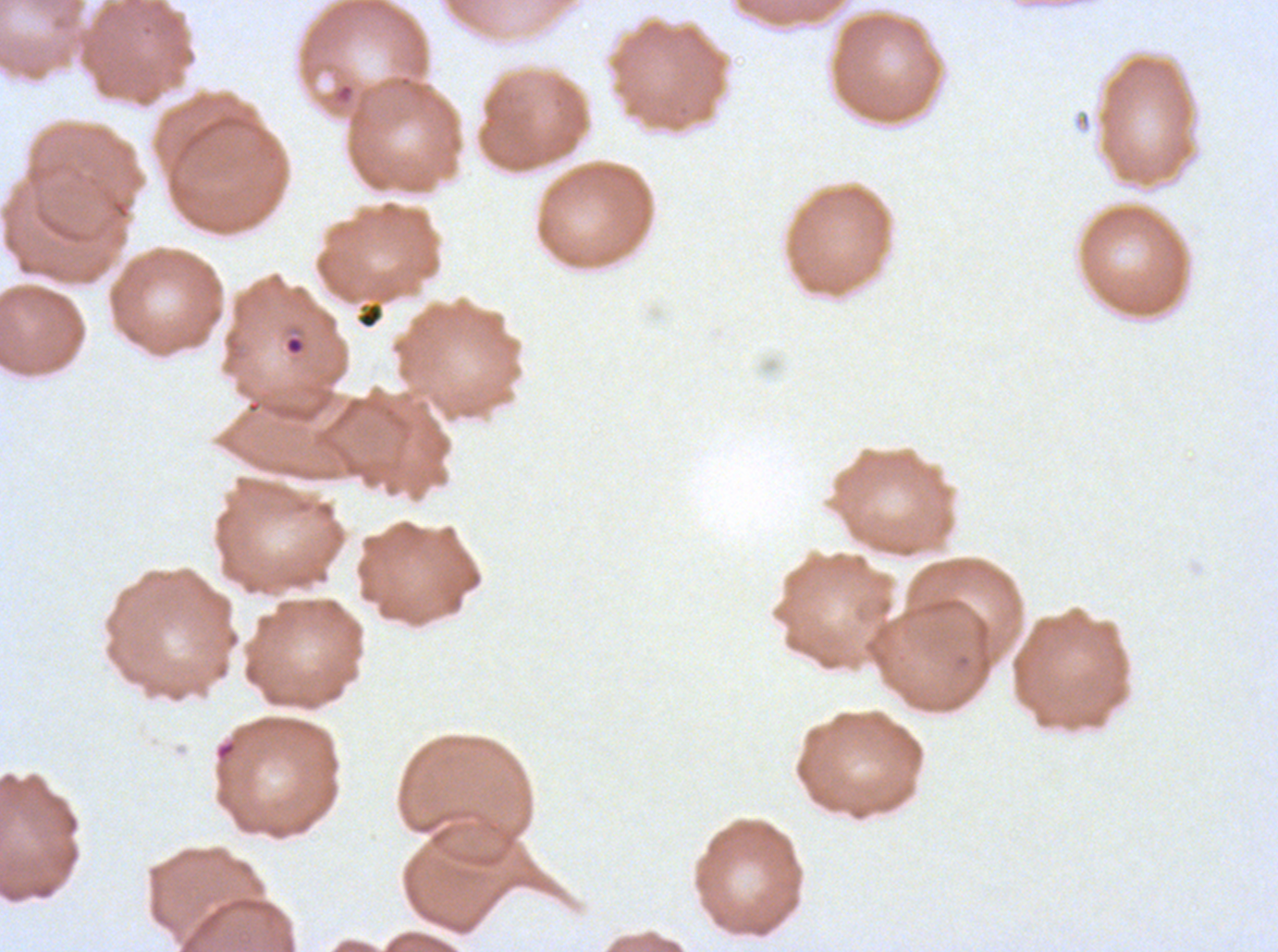
notation = approximate bounding boxes as [x1, y1, x2, y2] in pixels
ring locations = [284, 335, 305, 356]
debris locations = [333, 81, 355, 104], [355, 300, 385, 330], [214, 738, 238, 763]
image size = 1278×952 pixels
preparation = thin blood film
stain = Giemsa
field of view = one sub-image of a larger composite
specimen = P. falciparum cultured ex vivo for 24 to 48 hours, from a patient in The Gambia